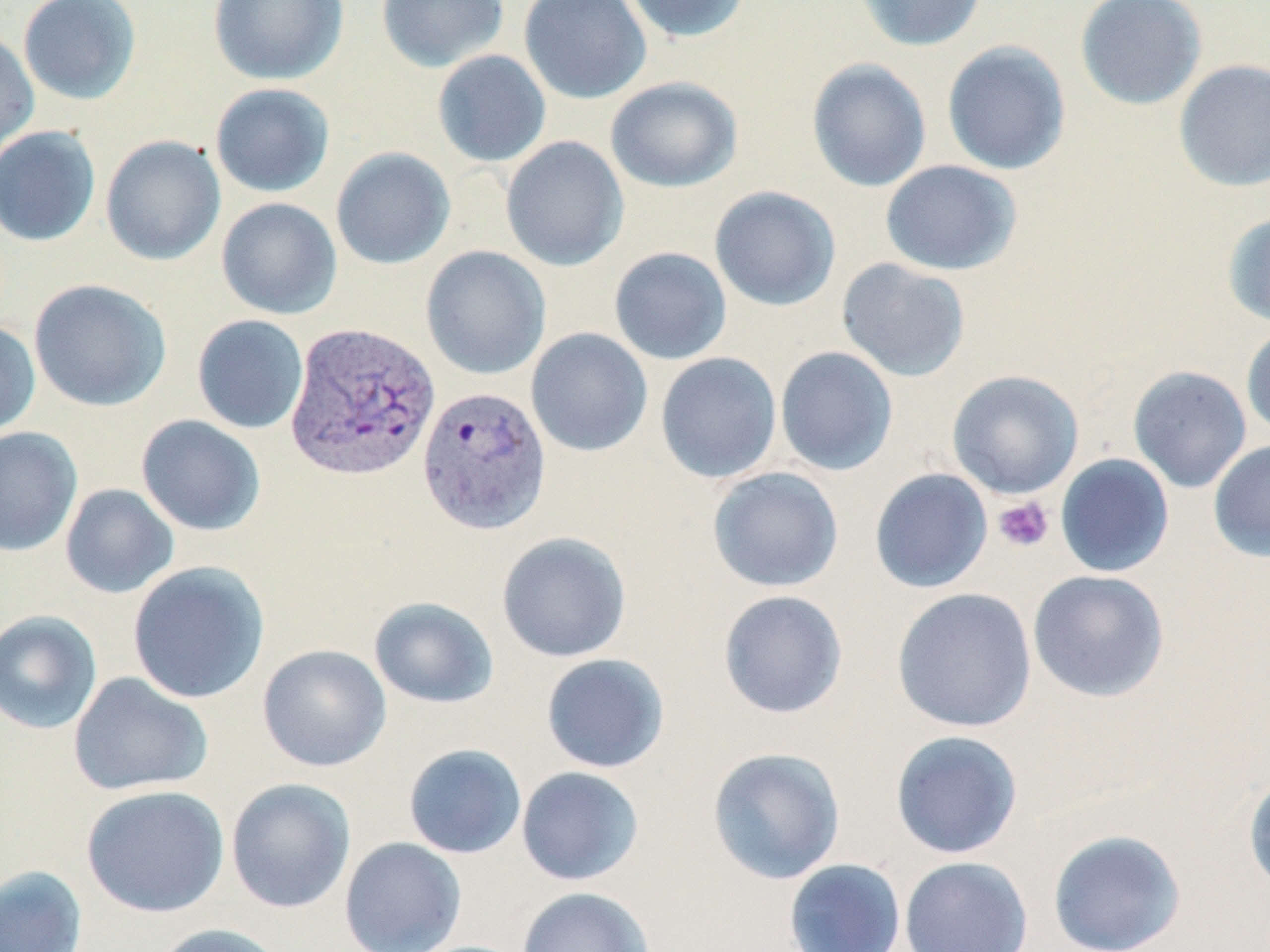 Approximate bounding boxes as (x1, y1, x2, y2) in pixels. Plasmodium vivax-infected red blood cell locations: (284, 322, 441, 482), (417, 385, 552, 535). Platelet locations: (992, 496, 1054, 553). Uninfected red blood cell locations: (18, 0, 142, 106), (208, 0, 348, 85), (376, 0, 509, 72), (519, 0, 651, 104), (620, 0, 753, 44), (852, 0, 988, 51), (1075, 0, 1208, 110), (0, 29, 39, 160), (941, 41, 1071, 175), (432, 50, 551, 168), (806, 58, 932, 193), (1173, 58, 1270, 192), (604, 76, 742, 193), (209, 83, 336, 198), (0, 125, 101, 247), (100, 135, 226, 266), (500, 136, 629, 272), (330, 147, 455, 270), (880, 160, 1022, 276), (709, 186, 841, 311), (216, 197, 342, 320), (1222, 212, 1270, 327), (420, 245, 551, 380), (608, 246, 732, 365), (836, 258, 971, 382), (29, 278, 171, 411), (192, 314, 309, 434), (0, 321, 41, 437), (1241, 325, 1270, 440), (526, 327, 653, 457), (775, 346, 898, 476), (655, 352, 782, 483), (1128, 365, 1252, 493), (947, 369, 1084, 499), (136, 415, 266, 537), (0, 426, 82, 557), (1208, 440, 1270, 562), (1055, 453, 1175, 577), (707, 467, 844, 593), (869, 468, 993, 593), (60, 483, 179, 599), (496, 531, 632, 663), (127, 561, 270, 704), (1027, 569, 1169, 703), (890, 587, 1038, 734), (717, 589, 849, 719), (368, 597, 499, 709), (0, 609, 103, 735), (257, 644, 391, 772), (540, 653, 670, 773), (68, 671, 213, 797), (889, 730, 1023, 859), (402, 743, 527, 859), (706, 747, 846, 885), (515, 766, 644, 885), (1243, 771, 1270, 897), (225, 777, 356, 913), (81, 784, 230, 918), (1047, 828, 1186, 952), (339, 837, 467, 952), (899, 856, 1033, 951), (782, 858, 906, 952), (0, 864, 87, 952), (516, 886, 654, 952), (152, 923, 288, 952). Slide-level diagnosis: Plasmodium vivax. May-Grünwald-Giemsa stain. Single field of view. 1000x magnification. Light microscopy. Image is 1270×952 pixels. Thin blood film.